Name the blood parasite species.
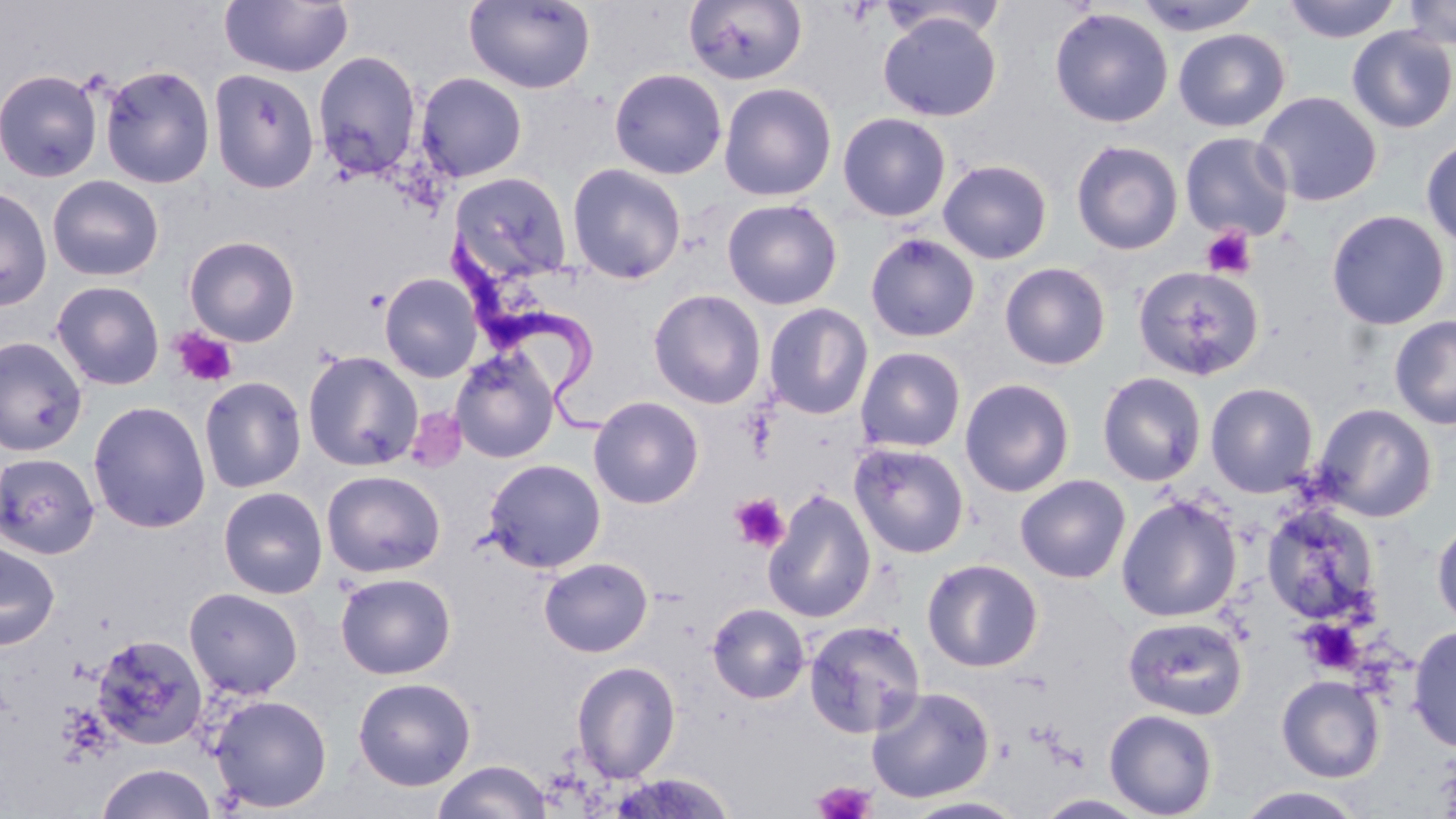
Trypanosoma brucei.

{
  "uninfected_red_blood_cell_locations": "approximate bounding boxes as (x1, y1, x2, y2) in pixels: (220, 0, 354, 78), (683, 0, 809, 86), (1131, 0, 1263, 36), (1283, 0, 1403, 43), (1400, 0, 1456, 50), (463, 1, 596, 94), (1049, 7, 1174, 128), (878, 11, 1002, 122), (1346, 26, 1456, 133), (1173, 29, 1290, 131), (312, 50, 423, 180), (99, 64, 216, 189), (609, 67, 727, 179), (208, 68, 320, 194), (0, 69, 103, 183), (416, 72, 528, 182), (718, 81, 837, 201), (1254, 91, 1382, 207), (837, 112, 952, 222), (1179, 131, 1294, 241), (1420, 136, 1456, 250), (1071, 140, 1183, 255), (938, 159, 1052, 264), (567, 162, 686, 284), (449, 171, 573, 284), (47, 174, 164, 282), (0, 185, 52, 311), (721, 199, 843, 310), (1326, 209, 1451, 330), (864, 232, 980, 343), (184, 235, 301, 346), (999, 262, 1111, 370), (1131, 265, 1264, 381), (378, 272, 484, 383), (51, 280, 165, 390), (648, 289, 766, 408), (764, 303, 873, 419), (1389, 315, 1456, 430), (0, 336, 88, 457), (856, 346, 966, 453), (450, 347, 560, 463), (303, 351, 423, 471), (1097, 371, 1207, 486), (198, 376, 307, 493), (959, 378, 1075, 497), (1205, 382, 1319, 497), (588, 396, 704, 509), (87, 400, 211, 533), (1311, 403, 1437, 522), (849, 442, 970, 559), (0, 451, 101, 559), (483, 458, 606, 572), (321, 469, 446, 578), (1015, 474, 1131, 583), (217, 486, 328, 599), (763, 489, 877, 624), (1116, 495, 1242, 623), (1260, 502, 1381, 624), (1431, 517, 1456, 632), (0, 541, 60, 650), (539, 557, 653, 657), (922, 558, 1043, 672), (335, 572, 456, 679), (183, 587, 304, 699), (707, 603, 810, 703), (1122, 616, 1249, 721), (803, 620, 926, 738), (1407, 624, 1456, 753), (90, 633, 208, 750), (571, 660, 681, 782), (1276, 674, 1385, 783), (352, 676, 476, 791), (866, 685, 995, 803), (208, 693, 333, 813), (1104, 708, 1218, 819), (432, 760, 552, 819), (95, 762, 217, 819), (608, 772, 736, 818), (1232, 786, 1370, 819), (900, 796, 1029, 819)",
  "image_size": "1456×819 pixels",
  "magnification": "1000x",
  "field_of_view": "one of a larger specimen",
  "platelet_locations": "approximate bounding boxes as (x1, y1, x2, y2) in pixels: (1202, 226, 1258, 279), (171, 328, 238, 388), (730, 493, 789, 553), (1299, 619, 1364, 675), (813, 779, 875, 819)",
  "modality": "light microscopy",
  "trypanosoma_brucei_locations": "approximate bounding boxes as (x1, y1, x2, y2) in pixels: (444, 228, 615, 439)",
  "stain": "May-Grünwald-Giemsa",
  "preparation": "thin blood film"
}